Assess this cell for malaria.
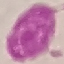
It is uninfected.

Acquired by smartphone through the microscope eyepiece. Thin smear of blood. Automatically extracted cell patch, resized to 64 × 64 pixels. Giemsa-stained preparation.